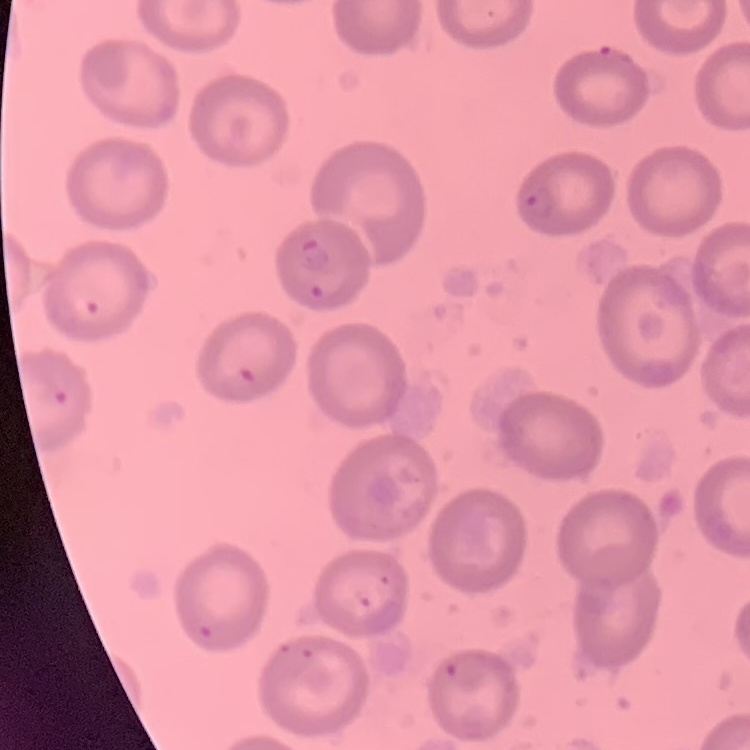

{
  "red_blood_cell_morphology": "no rouleaux formation",
  "image_type": "one tile cut from a larger photomicrograph",
  "stain": "Field's or Giemsa",
  "preparation": "thin blood smear"
}